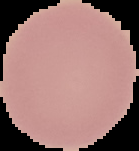

From a thin blood smear. Image is 139×151 pixels. Result: negative for malaria parasites. The area outside the segmented cell region is set to black.